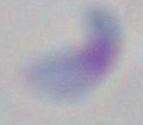

magnification = 1000x
identification = Toxoplasma gondii
modality = photomicrograph